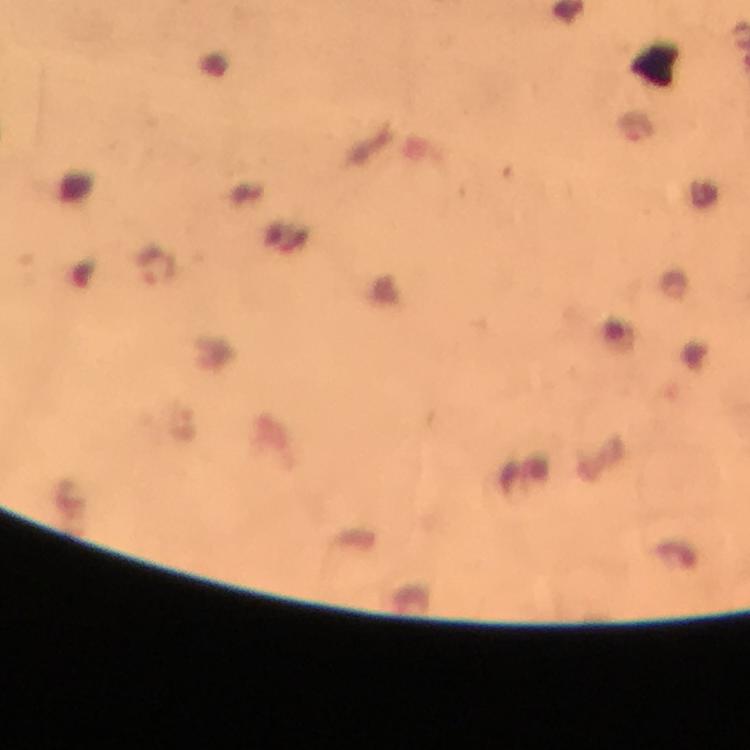 Approximate centers as [x, y] in pixels. Malaria parasite locations: [157, 267], [183, 426]. Immersion oil was used. From a diagnostic examination for malaria. Smartphone photograph taken through a microscope. At 100x magnification. Thick blood smear. Giemsa stain. Image is 750×750 pixels. Cropped region of a single field of view.